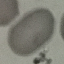

Summary:
  - Result: no malaria parasites detected
  - Stain: Giemsa
  - Preparation: thin smear
  - Image type: automatically extracted cell patch, resized to 64 × 64 pixels
  - Capture: smartphone through the microscope eyepiece